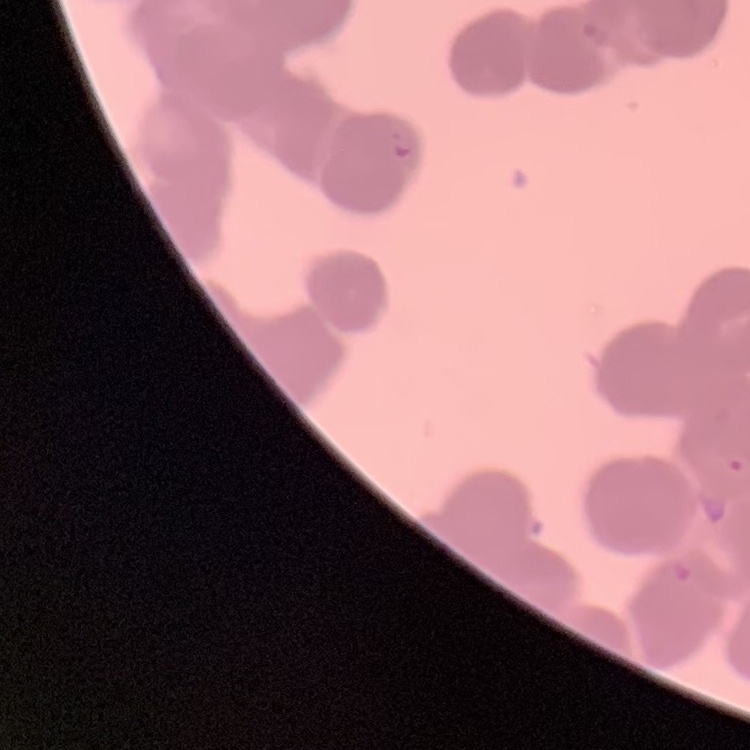 The red blood cells exhibit rouleaux formation. Field's or Giemsa stain. One tile cut from a larger photomicrograph. Thin peripheral smear.